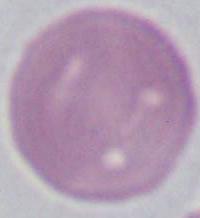
modality: micrograph
magnification: 1000x
identification: erythrocyte